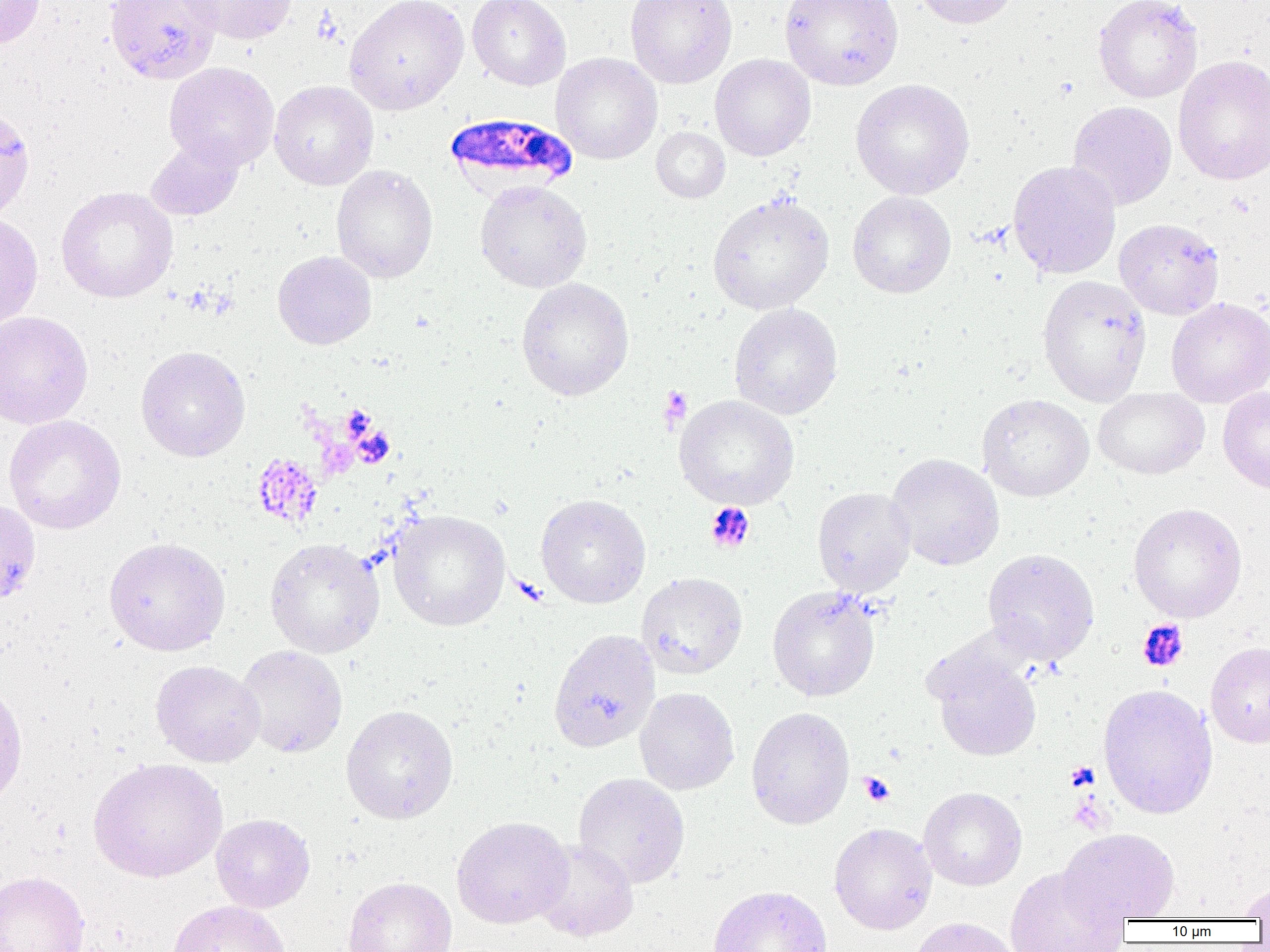 Approximate bounding boxes as named x1/y1/x2/y2 corners in pixels. Uninfected red blood cell locations: (x1=0, y1=0, x2=45, y2=49), (x1=104, y1=0, x2=222, y2=84), (x1=177, y1=0, x2=297, y2=44), (x1=344, y1=0, x2=469, y2=115), (x1=468, y1=0, x2=571, y2=90), (x1=625, y1=0, x2=737, y2=88), (x1=780, y1=0, x2=903, y2=91), (x1=913, y1=0, x2=1019, y2=28), (x1=1092, y1=0, x2=1203, y2=103), (x1=551, y1=53, x2=662, y2=164), (x1=709, y1=53, x2=816, y2=161), (x1=1172, y1=55, x2=1270, y2=186), (x1=164, y1=62, x2=279, y2=170), (x1=850, y1=78, x2=975, y2=199), (x1=269, y1=80, x2=378, y2=190), (x1=1067, y1=101, x2=1177, y2=210), (x1=0, y1=105, x2=35, y2=223), (x1=652, y1=127, x2=730, y2=203), (x1=144, y1=137, x2=245, y2=221), (x1=1007, y1=160, x2=1122, y2=279), (x1=331, y1=164, x2=439, y2=284), (x1=474, y1=179, x2=592, y2=293), (x1=55, y1=186, x2=178, y2=303), (x1=847, y1=191, x2=956, y2=298), (x1=707, y1=193, x2=834, y2=315), (x1=0, y1=213, x2=43, y2=330), (x1=1114, y1=218, x2=1225, y2=320), (x1=273, y1=250, x2=376, y2=349), (x1=1037, y1=274, x2=1152, y2=406), (x1=515, y1=277, x2=634, y2=400), (x1=1165, y1=297, x2=1270, y2=408), (x1=729, y1=303, x2=843, y2=419), (x1=0, y1=310, x2=93, y2=430), (x1=135, y1=345, x2=250, y2=462), (x1=1093, y1=387, x2=1209, y2=479), (x1=1218, y1=387, x2=1270, y2=495), (x1=977, y1=393, x2=1094, y2=501), (x1=674, y1=395, x2=799, y2=510), (x1=3, y1=414, x2=126, y2=535), (x1=886, y1=453, x2=1005, y2=571), (x1=812, y1=486, x2=916, y2=597), (x1=536, y1=494, x2=651, y2=608), (x1=0, y1=498, x2=41, y2=605), (x1=1128, y1=503, x2=1247, y2=622), (x1=388, y1=509, x2=510, y2=631), (x1=104, y1=537, x2=230, y2=656), (x1=264, y1=537, x2=384, y2=658), (x1=982, y1=548, x2=1100, y2=665), (x1=636, y1=571, x2=748, y2=679), (x1=767, y1=586, x2=880, y2=702), (x1=548, y1=628, x2=660, y2=752), (x1=1205, y1=642, x2=1270, y2=747), (x1=236, y1=645, x2=348, y2=758), (x1=929, y1=648, x2=1043, y2=762), (x1=151, y1=660, x2=265, y2=767), (x1=0, y1=682, x2=28, y2=810), (x1=1097, y1=684, x2=1218, y2=819), (x1=634, y1=687, x2=739, y2=795), (x1=341, y1=704, x2=458, y2=824), (x1=746, y1=706, x2=855, y2=829), (x1=88, y1=757, x2=227, y2=882), (x1=573, y1=773, x2=690, y2=888), (x1=919, y1=787, x2=1027, y2=891), (x1=210, y1=813, x2=315, y2=913), (x1=451, y1=816, x2=572, y2=929), (x1=829, y1=823, x2=937, y2=934), (x1=1059, y1=828, x2=1180, y2=923), (x1=532, y1=839, x2=639, y2=942), (x1=1004, y1=866, x2=1129, y2=952), (x1=0, y1=871, x2=90, y2=952), (x1=342, y1=876, x2=457, y2=952), (x1=1237, y1=882, x2=1270, y2=919), (x1=708, y1=885, x2=833, y2=952), (x1=166, y1=899, x2=290, y2=952), (x1=909, y1=916, x2=1020, y2=952). Plasmodium falciparum-infected red blood cell locations: (x1=445, y1=113, x2=577, y2=194). Platelet locations: (x1=659, y1=386, x2=692, y2=429), (x1=250, y1=453, x2=323, y2=529), (x1=705, y1=502, x2=756, y2=554), (x1=1137, y1=620, x2=1189, y2=673), (x1=1066, y1=761, x2=1099, y2=792), (x1=859, y1=771, x2=895, y2=807). Slide-level diagnosis: Plasmodium falciparum. One field of a larger specimen. 1000x magnification. Image is 1270×952 pixels. Optical microscopy. Thin blood film.